Name the cell type shown.
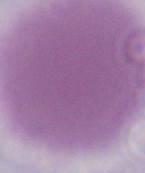
This is an erythrocyte.

Micrograph. 1000x magnification.